Report the malaria status of this cell.
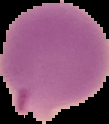
Parasitized.

Summary:
  - Preparation: thin blood smear
  - Image type: segmented cell region with the area outside set to black
  - Image size: 109×124 pixels